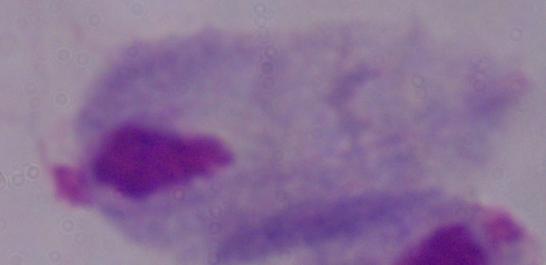
identification = trichomonad
magnification = 1000x
modality = photomicrograph